Assess this cell for malaria.
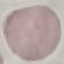

It is uninfected.

stain = Giemsa
preparation = thin blood smear
capture = smartphone camera at the microscope eyepiece
image type = cell patch, automatically extracted from a larger field of view and resized to 64 × 64 pixels